Point out every malaria parasite.
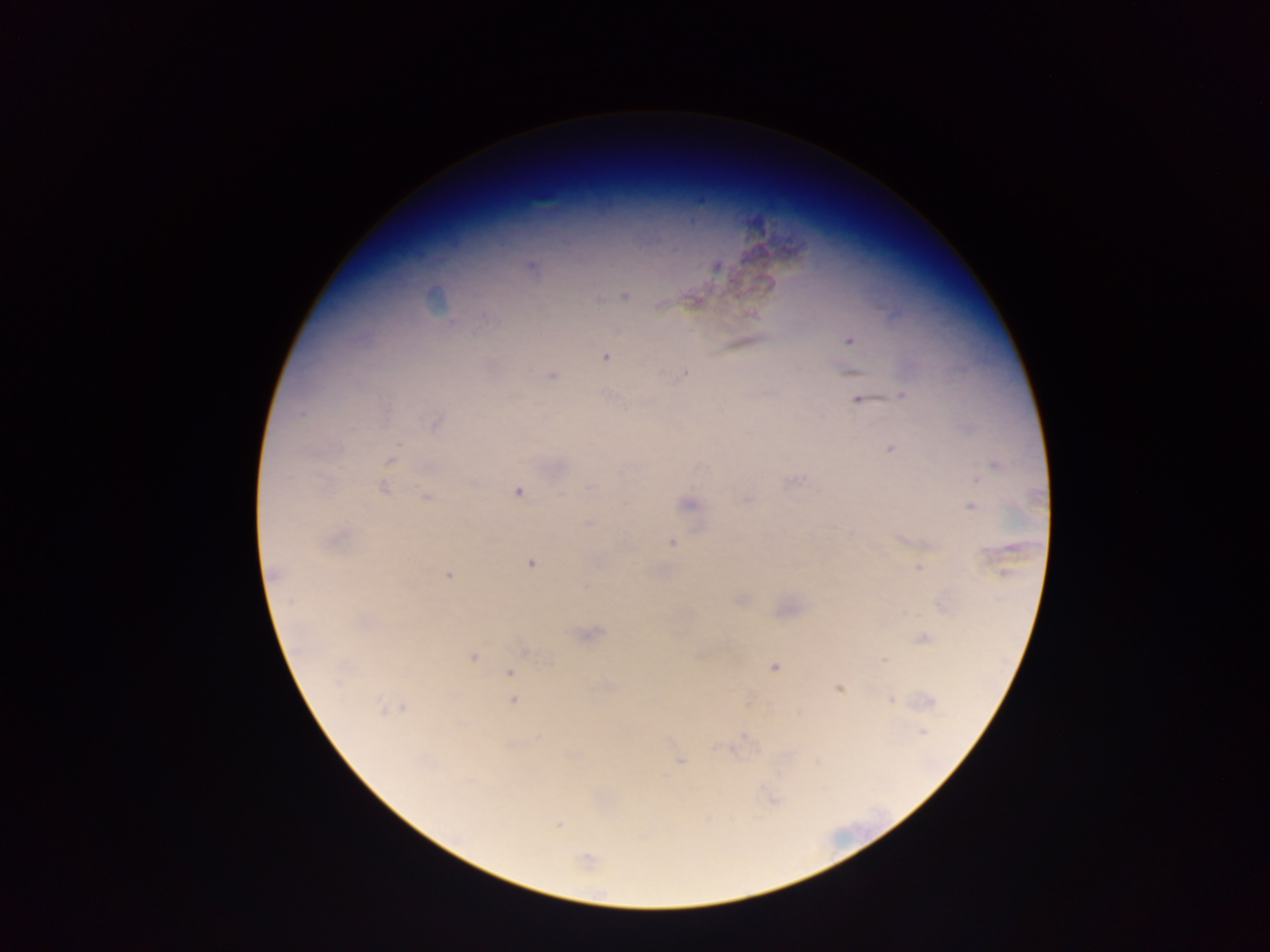
Approximate centers as (x, y) in pixels.
Malaria parasites: (532, 267), (625, 295), (599, 299), (660, 305), (753, 313), (849, 340), (605, 357), (684, 373), (553, 374), (902, 395), (859, 399), (302, 413), (435, 422), (891, 448), (390, 460), (994, 464), (794, 482), (384, 487), (589, 487), (518, 492), (426, 496), (747, 499), (689, 503), (971, 506), (588, 524), (338, 537), (671, 542), (531, 563), (919, 567), (275, 573), (448, 576), (592, 634), (923, 638), (525, 650), (472, 657), (884, 661), (774, 667), (510, 673), (839, 688), (891, 700), (512, 701), (931, 702), (403, 707), (381, 708), (922, 731), (680, 761), (558, 825), (586, 859).

field of view = single
country = Ghana
capture = mobile-phone photograph through a microscope
preparation = thick blood smear
image size = 1270×952 pixels